Identify the parasite.
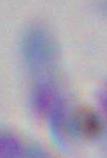

Toxoplasma gondii.

Summary:
  - Modality: micrograph
  - Magnification: 1000x